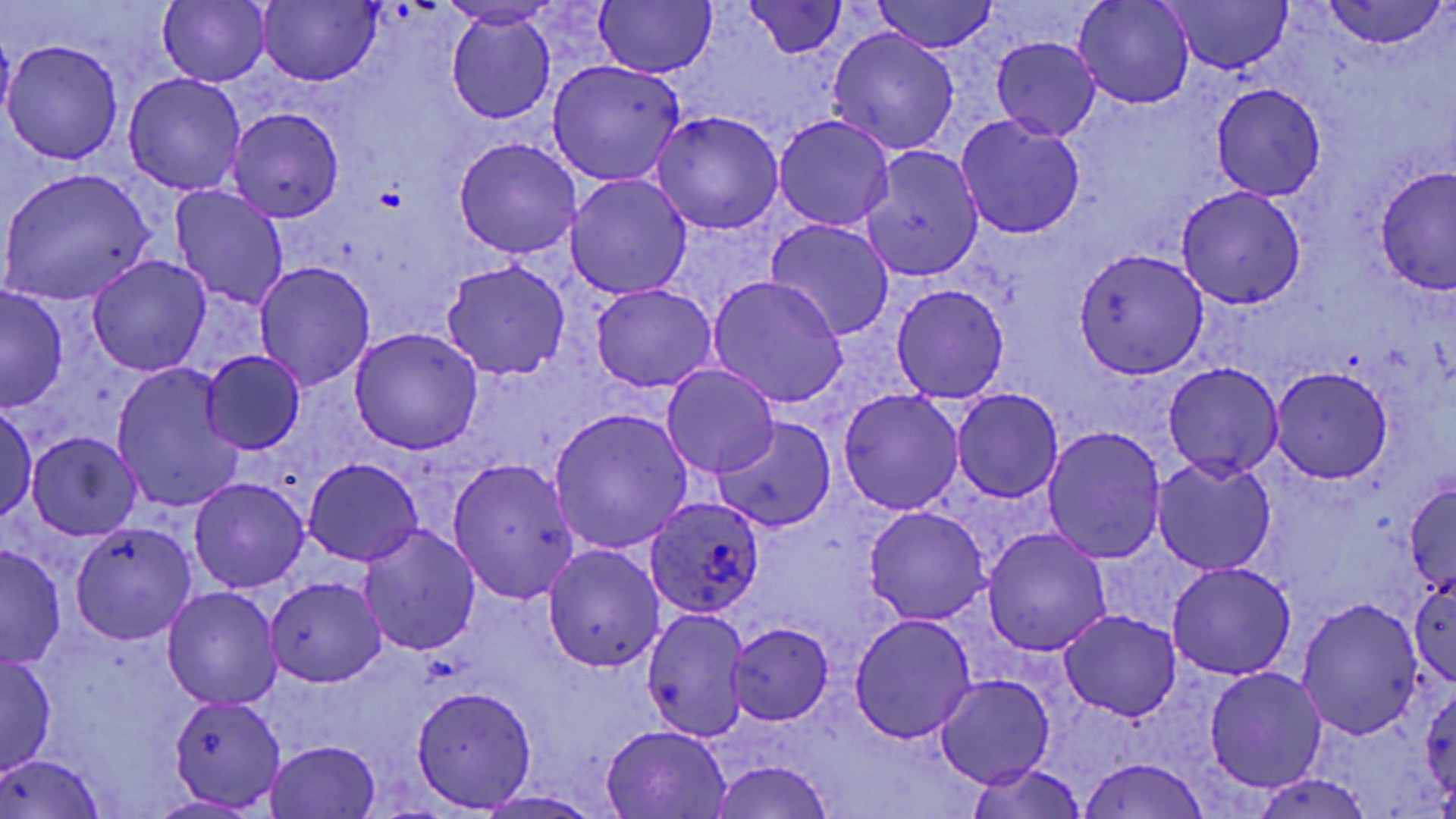

{
  "slide_level_diagnosis": "Plasmodium ovale",
  "field_of_view": "single",
  "magnification": "1000x",
  "plasmodium_ovale_infected_red_blood_cell_locations": "approximate bounding boxes as [x1, y1, x2, y2] in pixels: [646, 496, 767, 620]",
  "preparation": "thin blood smear",
  "platelet_locations": "approximate bounding boxes as [x1, y1, x2, y2] in pixels: [375, 186, 404, 211]",
  "modality": "optical microscopy",
  "uninfected_red_blood_cell_locations": "approximate bounding boxes as [x1, y1, x2, y2] in pixels: [158, 0, 271, 87], [258, 0, 381, 86], [870, 0, 1001, 53], [1162, 0, 1296, 73], [594, 1, 716, 78], [1074, 1, 1195, 109], [1322, 1, 1447, 49], [746, 2, 849, 58], [446, 11, 556, 125], [1, 27, 16, 135], [826, 27, 960, 154], [991, 37, 1101, 140], [3, 40, 124, 164], [546, 59, 685, 185], [124, 73, 246, 195], [1212, 83, 1327, 200], [228, 108, 344, 222], [651, 111, 784, 235], [773, 114, 894, 231], [956, 116, 1086, 238], [452, 137, 584, 260], [859, 146, 984, 281], [1375, 167, 1455, 295], [1, 169, 155, 306], [565, 174, 692, 300], [169, 185, 290, 311], [1176, 186, 1306, 309], [765, 218, 895, 340], [1073, 248, 1210, 378], [88, 254, 211, 376], [441, 260, 569, 380], [254, 262, 375, 392], [706, 275, 849, 409], [590, 283, 717, 392], [890, 284, 1009, 404], [0, 287, 68, 411], [349, 328, 483, 455], [199, 350, 307, 455], [1163, 360, 1284, 481], [662, 364, 780, 477], [110, 365, 244, 513], [1270, 366, 1394, 484], [838, 388, 963, 515], [953, 388, 1063, 502], [0, 401, 38, 523], [548, 407, 693, 556], [712, 416, 837, 533], [1044, 425, 1168, 562], [26, 432, 141, 539], [448, 457, 580, 606], [1152, 457, 1276, 573], [303, 458, 423, 567], [189, 477, 308, 593], [1403, 480, 1455, 596], [864, 506, 991, 625], [70, 520, 200, 644], [358, 523, 481, 656], [981, 528, 1111, 655], [0, 543, 66, 669], [542, 545, 664, 672], [1165, 562, 1296, 680], [1408, 574, 1455, 687], [266, 576, 386, 686], [163, 587, 282, 710], [1295, 598, 1424, 742], [641, 607, 752, 743], [1058, 611, 1181, 723], [850, 615, 977, 743], [727, 623, 833, 726], [0, 652, 57, 775], [1205, 667, 1326, 792], [936, 674, 1055, 788], [1422, 684, 1456, 804], [411, 686, 537, 812], [168, 694, 288, 811], [600, 723, 732, 817], [266, 740, 381, 817], [2, 752, 103, 818], [1076, 757, 1213, 818], [706, 760, 836, 819], [965, 762, 1088, 819], [1252, 772, 1375, 818], [473, 792, 609, 818]",
  "stain": "May-Grünwald-Giemsa",
  "image_size": "1456×819 pixels"
}